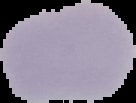

{
  "preparation": "thin blood film",
  "image_type": "cell region segmented out of the field of view; surrounding area masked to black",
  "malaria_status": "uninfected",
  "image_size": "136×103 pixels"
}